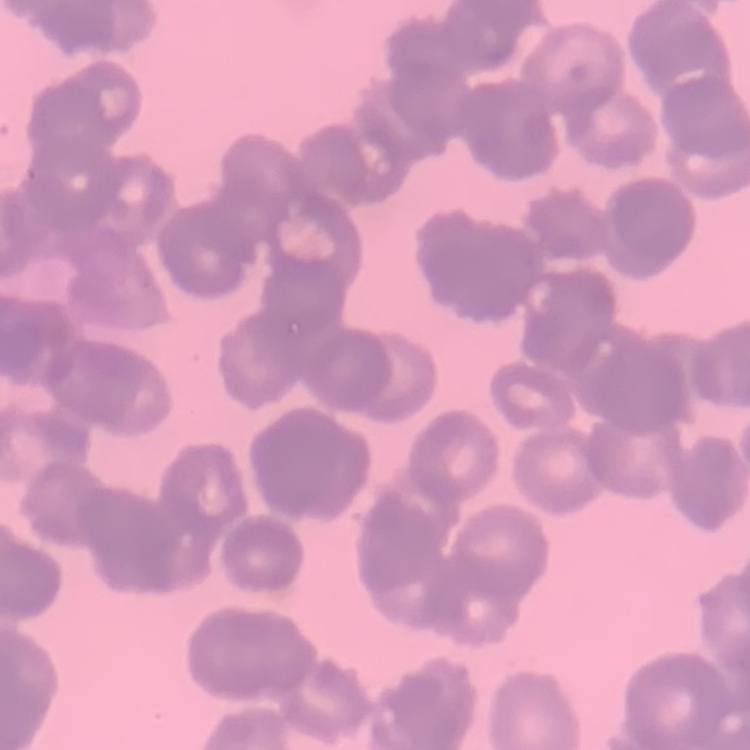
{
  "erythrocyte_morphology": "rouleaux formation",
  "image_type": "square crop of a larger photomicrograph",
  "stain": "Field's or Giemsa",
  "preparation": "thin peripheral smear"
}